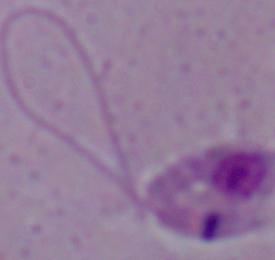
A Leishmania parasite is shown. Captured at 1000x magnification. Photomicrograph.